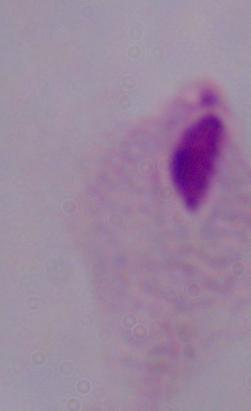 Photomicrograph. A trichomonad is shown. 1000x magnification.